Describe the morphology of the erythrocytes.
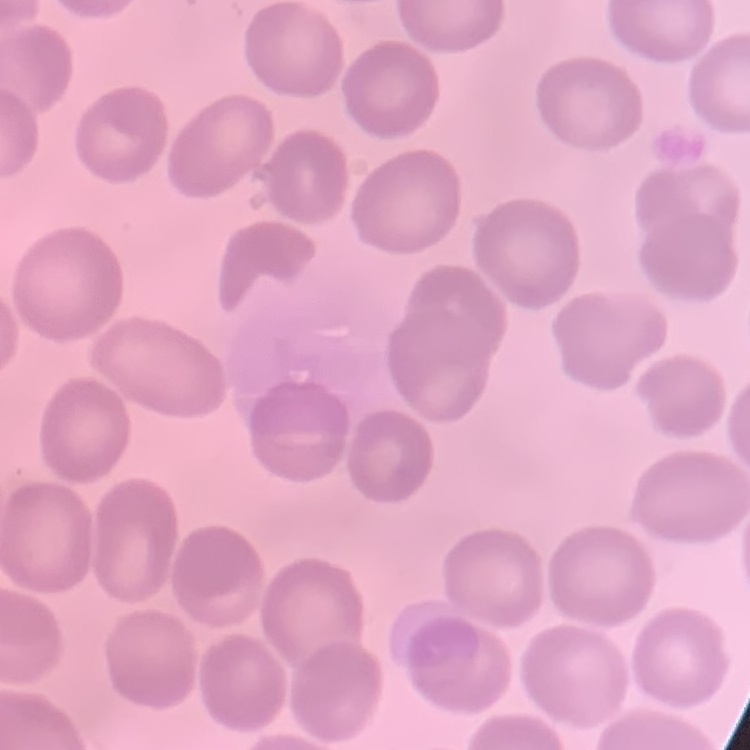

No rouleaux formation.

One tile cut from a larger photomicrograph. Thin blood smear. Field's or Giemsa stain.